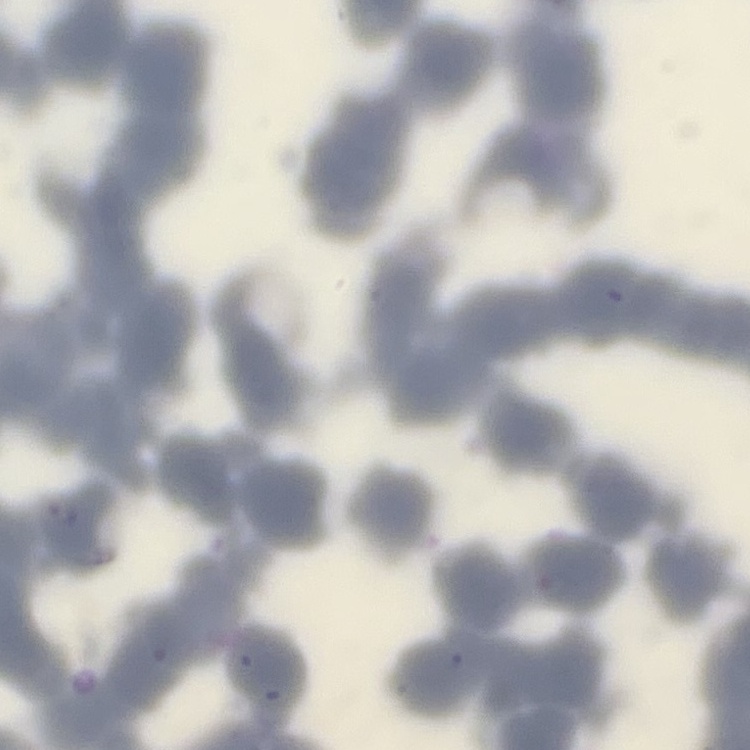

The red blood cells show rouleaux formation. Field's or Giemsa stain. Square crop of a larger photomicrograph. Thin peripheral smear.